State which parasite is depicted.
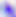
This is Toxoplasma gondii.

Summary:
  - Magnification: 400x
  - Modality: photomicrograph